Name the blood parasite species.
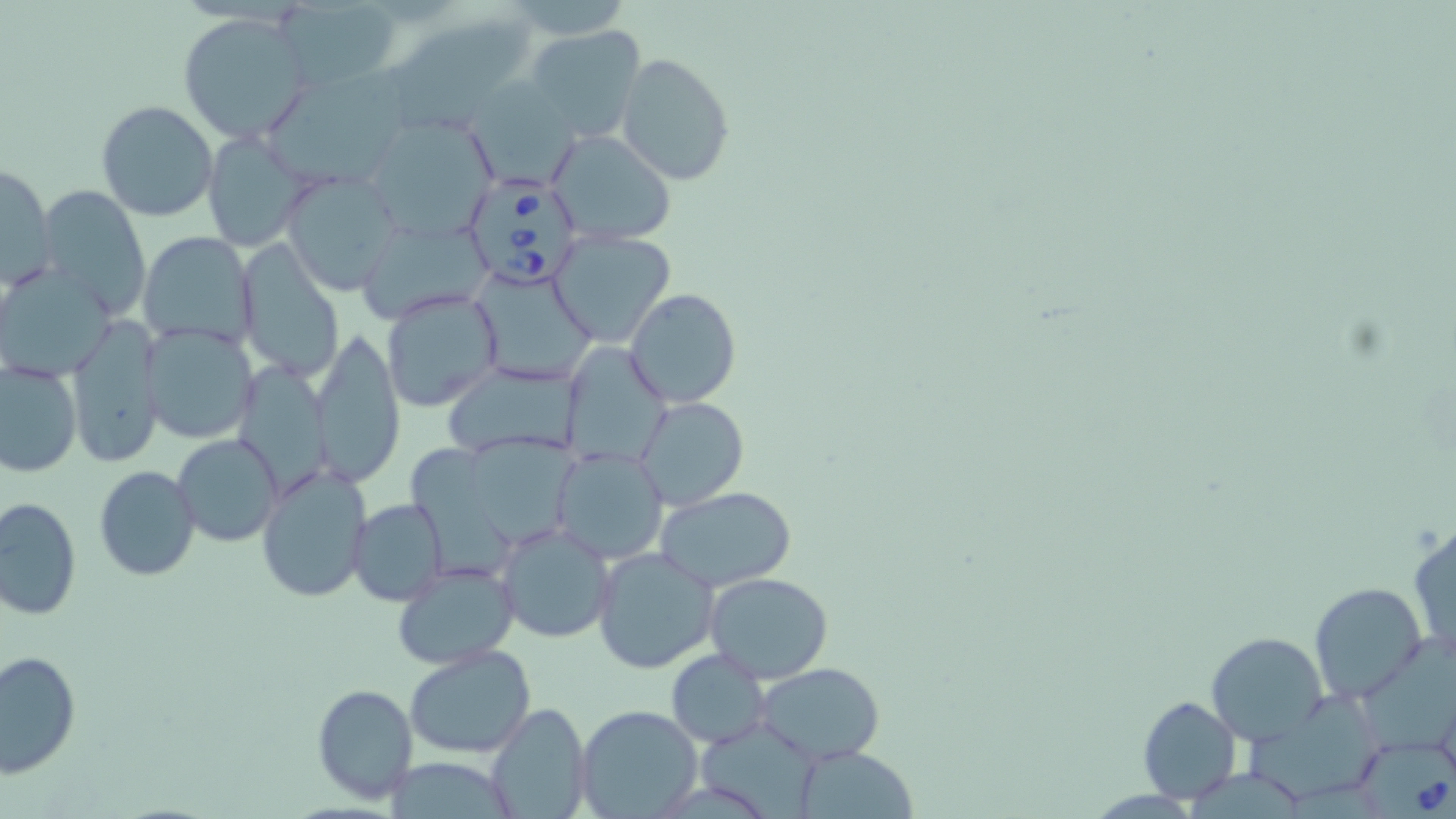
Babesia divergens.

modality = light microscopy
Babesia divergens-infected red blood cell locations = approximate bounding boxes as [x1, y1, x2, y2] in pixels: [461, 172, 585, 292], [1354, 744, 1456, 818]
uninfected red blood cell locations = approximate bounding boxes as [x1, y1, x2, y2] in pixels: [279, 0, 401, 91], [179, 13, 312, 144], [383, 16, 536, 130], [525, 24, 646, 143], [615, 52, 736, 186], [271, 56, 418, 184], [466, 78, 579, 190], [96, 100, 219, 222], [362, 114, 497, 242], [544, 128, 678, 246], [201, 130, 315, 252], [0, 162, 56, 287], [282, 171, 407, 297], [39, 183, 151, 317], [357, 216, 494, 326], [548, 229, 677, 349], [139, 232, 257, 352], [237, 242, 346, 381], [1, 262, 118, 379], [471, 265, 599, 386], [380, 287, 505, 414], [625, 288, 742, 407], [68, 313, 162, 468], [142, 322, 263, 445], [310, 329, 406, 487], [559, 341, 671, 468], [2, 360, 81, 477], [237, 360, 342, 492], [442, 361, 586, 460], [636, 396, 748, 511], [173, 433, 283, 547], [471, 437, 574, 546], [405, 444, 520, 578], [549, 447, 668, 564], [257, 463, 374, 603], [95, 465, 200, 581], [655, 485, 797, 591], [0, 495, 81, 622], [348, 498, 448, 606], [1408, 517, 1455, 664], [496, 523, 614, 644], [592, 548, 720, 674], [393, 561, 520, 671], [704, 572, 834, 682], [1309, 582, 1428, 704], [1206, 631, 1327, 744], [1365, 635, 1456, 767], [403, 645, 534, 758], [665, 649, 769, 749], [2, 650, 79, 778], [754, 662, 884, 763], [312, 683, 419, 804], [1137, 695, 1241, 804], [1253, 701, 1384, 794], [485, 702, 591, 818], [577, 705, 704, 819], [702, 724, 816, 819], [794, 746, 919, 817]
preparation = thin blood film
field of view = one of a larger specimen
image size = 1456×819 pixels
magnification = 1000x
stain = May-Grünwald-Giemsa